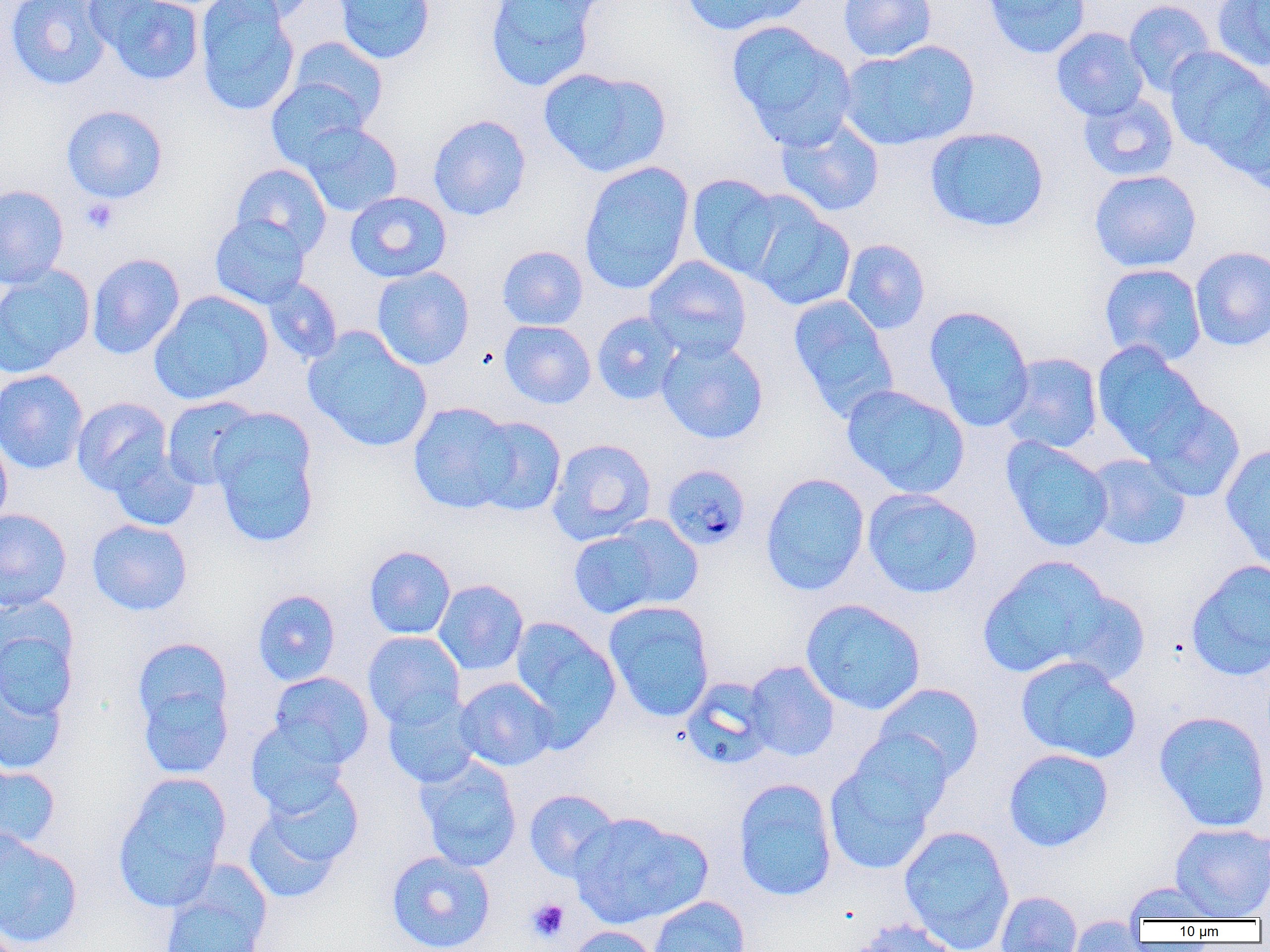
Summary:
  - Coordinate format: approximate bounding boxes as named x1/y1/x2/y2 corners in pixels
  - Platelet locations: (x1=80, y1=197, x2=119, y2=234), (x1=526, y1=898, x2=570, y2=942)
  - Plasmodium malariae-infected red blood cell locations: (x1=661, y1=463, x2=751, y2=550)
  - Uninfected red blood cell locations: (x1=5, y1=0, x2=112, y2=91), (x1=89, y1=0, x2=204, y2=86), (x1=194, y1=0, x2=300, y2=116), (x1=213, y1=0, x2=319, y2=24), (x1=332, y1=0, x2=436, y2=64), (x1=484, y1=0, x2=602, y2=91), (x1=679, y1=0, x2=810, y2=36), (x1=838, y1=0, x2=937, y2=62), (x1=982, y1=0, x2=1092, y2=59), (x1=1124, y1=0, x2=1216, y2=96), (x1=1212, y1=0, x2=1270, y2=72), (x1=727, y1=20, x2=857, y2=148), (x1=1051, y1=26, x2=1149, y2=121), (x1=287, y1=36, x2=388, y2=129), (x1=838, y1=40, x2=980, y2=151), (x1=1163, y1=47, x2=1269, y2=163), (x1=538, y1=66, x2=673, y2=178), (x1=266, y1=78, x2=369, y2=170), (x1=1231, y1=83, x2=1270, y2=195), (x1=1078, y1=92, x2=1179, y2=182), (x1=61, y1=104, x2=168, y2=204), (x1=427, y1=114, x2=532, y2=221), (x1=775, y1=115, x2=885, y2=217), (x1=297, y1=121, x2=404, y2=217), (x1=924, y1=125, x2=1049, y2=233), (x1=578, y1=160, x2=694, y2=295), (x1=230, y1=163, x2=332, y2=257), (x1=1089, y1=169, x2=1202, y2=272), (x1=686, y1=173, x2=787, y2=281), (x1=0, y1=184, x2=69, y2=288), (x1=344, y1=191, x2=452, y2=283), (x1=744, y1=199, x2=856, y2=311), (x1=210, y1=214, x2=311, y2=309), (x1=841, y1=239, x2=930, y2=334), (x1=497, y1=245, x2=588, y2=330), (x1=1189, y1=246, x2=1270, y2=351), (x1=86, y1=252, x2=185, y2=360), (x1=643, y1=255, x2=752, y2=361), (x1=1099, y1=263, x2=1207, y2=366), (x1=0, y1=265, x2=95, y2=378), (x1=371, y1=266, x2=475, y2=370), (x1=261, y1=277, x2=343, y2=365), (x1=149, y1=291, x2=273, y2=405), (x1=787, y1=294, x2=899, y2=422), (x1=924, y1=305, x2=1035, y2=431), (x1=591, y1=311, x2=684, y2=405), (x1=499, y1=320, x2=596, y2=409), (x1=302, y1=326, x2=433, y2=453), (x1=656, y1=336, x2=769, y2=444), (x1=1092, y1=342, x2=1209, y2=461), (x1=1001, y1=352, x2=1103, y2=453), (x1=0, y1=369, x2=88, y2=475), (x1=841, y1=384, x2=970, y2=498), (x1=1139, y1=395, x2=1247, y2=502), (x1=72, y1=396, x2=173, y2=495), (x1=161, y1=396, x2=262, y2=490), (x1=407, y1=401, x2=519, y2=515), (x1=207, y1=410, x2=321, y2=550), (x1=468, y1=415, x2=567, y2=516), (x1=0, y1=429, x2=12, y2=530), (x1=1002, y1=437, x2=1114, y2=552), (x1=547, y1=438, x2=656, y2=545), (x1=1220, y1=444, x2=1270, y2=569), (x1=107, y1=447, x2=200, y2=532), (x1=1085, y1=454, x2=1191, y2=551), (x1=760, y1=472, x2=870, y2=596), (x1=862, y1=488, x2=983, y2=599), (x1=0, y1=508, x2=72, y2=611), (x1=604, y1=515, x2=704, y2=611), (x1=86, y1=518, x2=193, y2=616), (x1=568, y1=525, x2=674, y2=620), (x1=364, y1=545, x2=456, y2=639), (x1=978, y1=555, x2=1118, y2=681), (x1=1186, y1=559, x2=1270, y2=681), (x1=433, y1=579, x2=528, y2=676), (x1=252, y1=589, x2=341, y2=686), (x1=1057, y1=589, x2=1152, y2=686), (x1=0, y1=597, x2=81, y2=722), (x1=800, y1=598, x2=927, y2=716), (x1=604, y1=600, x2=715, y2=722), (x1=509, y1=616, x2=622, y2=747), (x1=363, y1=631, x2=466, y2=729), (x1=132, y1=640, x2=236, y2=775), (x1=1015, y1=655, x2=1142, y2=765), (x1=743, y1=660, x2=840, y2=762), (x1=0, y1=665, x2=71, y2=776), (x1=268, y1=671, x2=374, y2=770), (x1=454, y1=676, x2=557, y2=771), (x1=680, y1=676, x2=777, y2=769), (x1=873, y1=682, x2=985, y2=783), (x1=381, y1=692, x2=482, y2=789), (x1=1153, y1=710, x2=1270, y2=833), (x1=245, y1=721, x2=349, y2=816), (x1=1003, y1=748, x2=1114, y2=852), (x1=824, y1=750, x2=944, y2=877), (x1=415, y1=757, x2=523, y2=871), (x1=0, y1=764, x2=60, y2=856), (x1=112, y1=772, x2=232, y2=913), (x1=243, y1=775, x2=364, y2=902), (x1=733, y1=777, x2=838, y2=902), (x1=524, y1=788, x2=621, y2=882), (x1=569, y1=812, x2=711, y2=929), (x1=1169, y1=822, x2=1270, y2=919), (x1=898, y1=825, x2=1015, y2=951), (x1=0, y1=830, x2=83, y2=950), (x1=386, y1=850, x2=496, y2=952), (x1=159, y1=874, x2=271, y2=952), (x1=1121, y1=881, x2=1228, y2=921), (x1=995, y1=890, x2=1083, y2=952), (x1=647, y1=896, x2=750, y2=952), (x1=1067, y1=915, x2=1147, y2=951), (x1=850, y1=918, x2=962, y2=952), (x1=566, y1=925, x2=660, y2=952)
  - Slide-level diagnosis: Plasmodium malariae
  - Magnification: 1000x
  - Preparation: thin blood film
  - Field of view: one of a larger specimen
  - Image size: 1270×952 pixels
  - Modality: optical microscopy